Comment on the morphology of the erythrocytes.
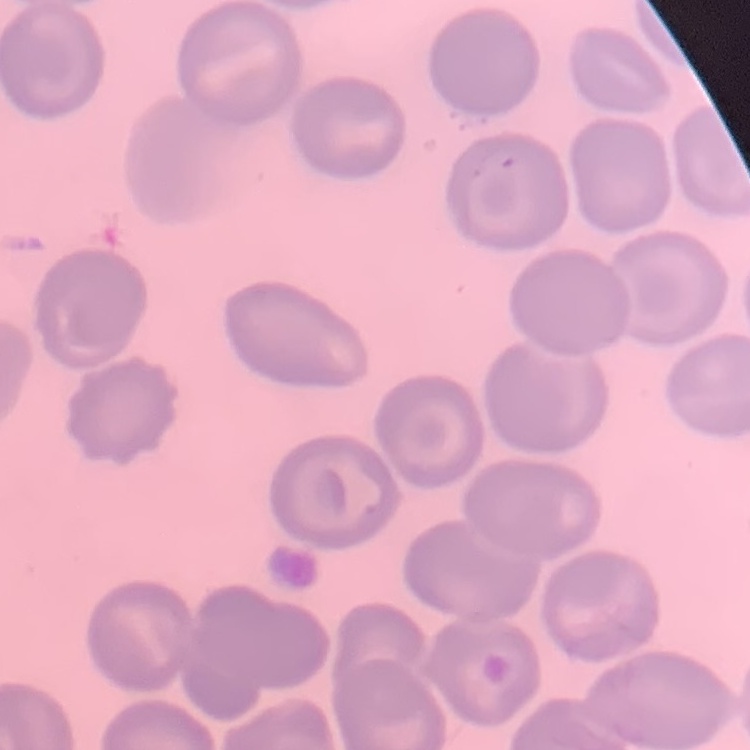

No rouleaux formation.

Thin blood smear. One tile cut from a larger photomicrograph. Stained with either Field's or Giemsa.